Classify this cell by malaria status.
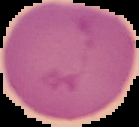
Uninfected.

Segmented cell region on a black background. Image is 139×127 pixels. From a thin blood smear.